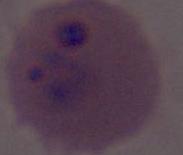
modality = micrograph
identification = Plasmodium
magnification = 400x or 1000x